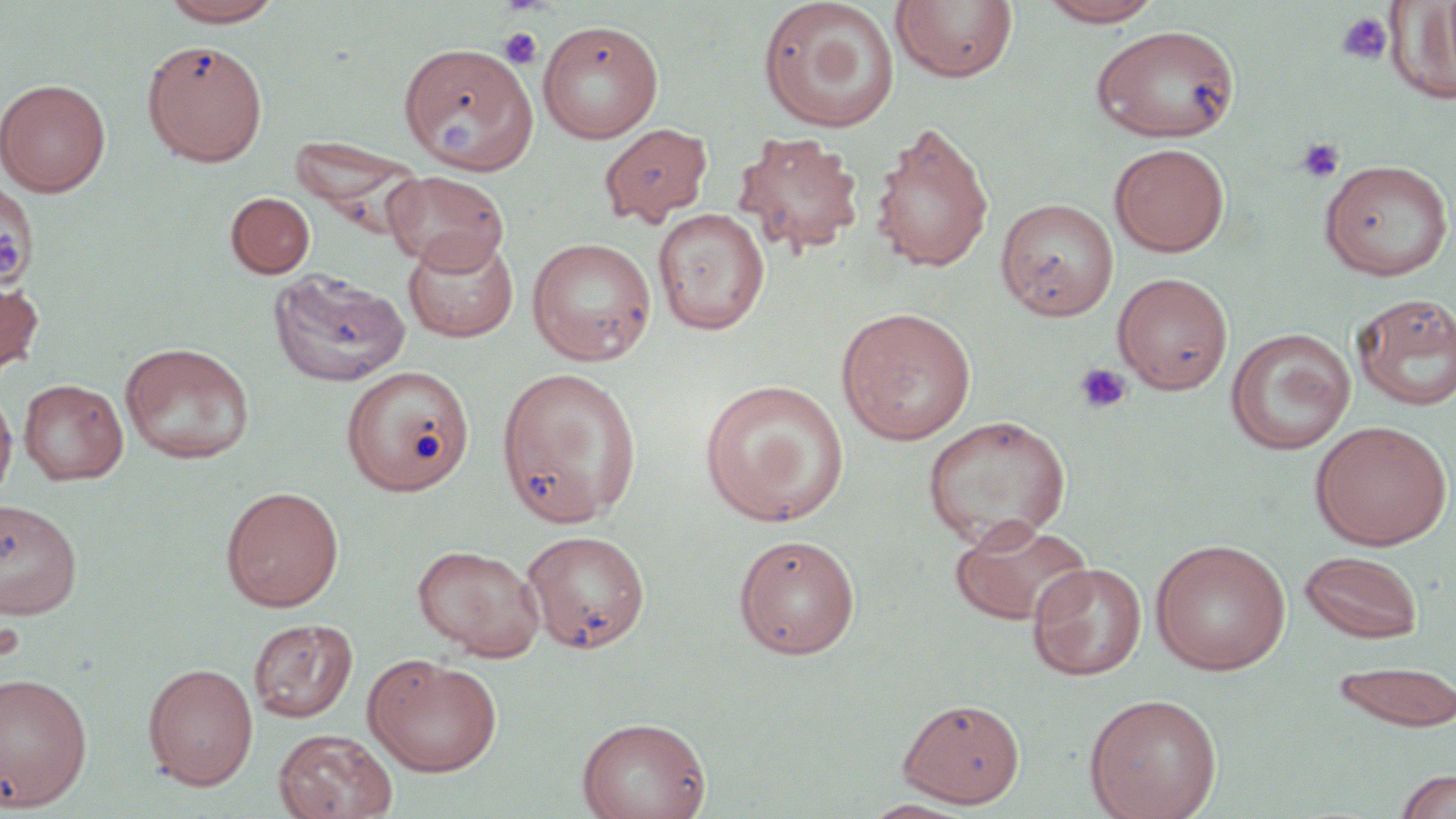 Approximate bounding boxes as (x1,y1)-(x2,y2) corner pairs in pixels. Platelet locations: (1335,12)-(1393,65), (499,26)-(543,70), (1296,137)-(1345,183), (0,229)-(30,282), (1073,362)-(1132,415), (0,619)-(25,663). Uninfected red blood cell locations: (157,0)-(286,27), (757,0)-(901,134), (890,1)-(1019,85), (1035,1)-(1166,27), (1386,1)-(1456,104), (537,20)-(664,143), (1090,24)-(1241,143), (143,40)-(268,166), (398,41)-(539,173), (0,78)-(111,197), (870,121)-(994,274), (599,122)-(713,227), (733,130)-(865,257), (290,136)-(429,234), (1109,143)-(1230,257), (1319,159)-(1454,281), (382,170)-(509,272), (0,182)-(39,300), (226,192)-(315,279), (995,198)-(1119,320), (653,207)-(770,335), (402,231)-(520,343), (527,236)-(657,365), (270,268)-(410,388), (1113,272)-(1234,395), (0,275)-(43,383), (1351,292)-(1456,412), (836,307)-(977,445), (1225,328)-(1356,455), (119,342)-(255,465), (340,365)-(474,496), (496,367)-(643,524), (18,378)-(128,485), (698,378)-(850,527), (0,386)-(17,507), (922,414)-(1072,549), (1310,419)-(1453,550), (221,486)-(344,611), (0,498)-(83,619), (949,516)-(1094,627), (521,529)-(651,654), (733,533)-(861,658), (1150,538)-(1291,675), (412,543)-(547,660), (1300,550)-(1424,644), (1028,562)-(1146,681), (248,618)-(359,722), (363,653)-(503,777), (1331,660)-(1455,732), (142,662)-(258,791), (0,672)-(93,811), (1084,693)-(1222,819), (897,697)-(1025,807), (576,716)-(711,819), (273,728)-(398,818), (1393,768)-(1456,819), (861,798)-(976,818). Slide-level diagnosis: negative for blood parasites. Image is 1456×819 pixels. Thin blood film. One field of a larger specimen. May-Grünwald-Giemsa-stained preparation. Optical microscopy. Captured at 1000x magnification.